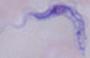

{
  "modality": "micrograph",
  "magnification": "1000x",
  "identification": "trypanosome"
}